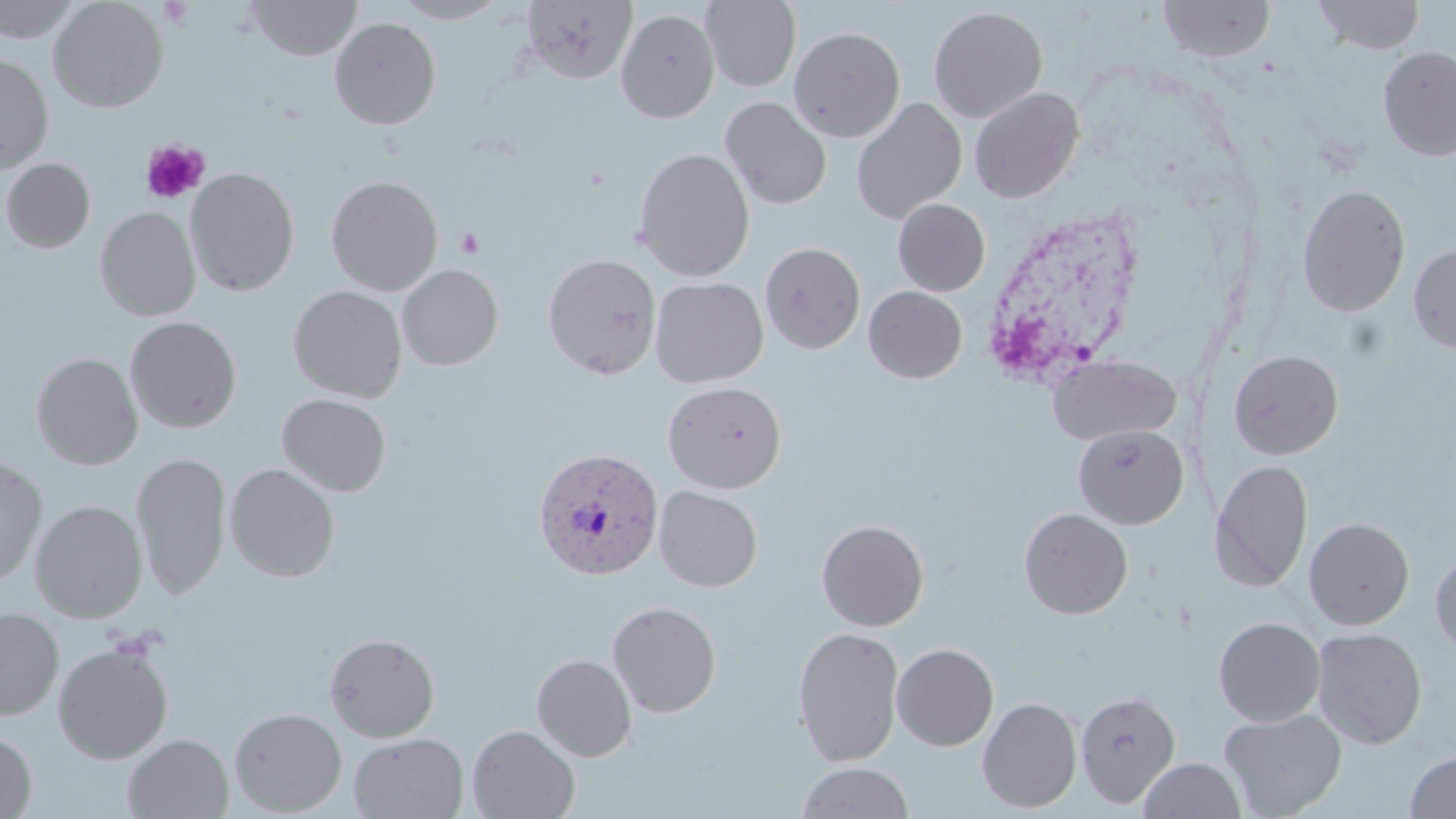
Summary:
  - Coordinate format: approximate bounding boxes as (x1,y1)-(x2,y2) corner pairs in pixels
  - Uninfected red blood cell locations: (48,0)-(168,113), (247,0)-(361,60), (392,0)-(507,23), (520,0)-(637,84), (701,0)-(800,91), (1159,0)-(1274,61), (1314,0)-(1424,54), (0,1)-(81,44), (929,6)-(1048,123), (616,9)-(719,123), (330,17)-(440,129), (789,26)-(904,142), (1378,46)-(1456,160), (0,55)-(54,173), (968,87)-(1085,203), (721,97)-(832,209), (850,98)-(967,225), (633,148)-(755,282), (0,158)-(95,252), (185,167)-(299,296), (326,175)-(443,296), (1297,184)-(1410,316), (893,199)-(990,296), (95,206)-(200,321), (760,243)-(865,354), (1408,244)-(1456,353), (543,254)-(662,379), (397,264)-(503,370), (649,277)-(768,388), (288,285)-(407,403), (864,286)-(966,383), (125,316)-(241,433), (1228,350)-(1343,459), (31,352)-(143,470), (1047,354)-(1181,445), (662,381)-(786,493), (277,394)-(391,497), (1073,424)-(1189,529), (131,452)-(231,599), (0,455)-(47,590), (1209,459)-(1313,592), (225,463)-(340,582), (654,485)-(762,591), (30,500)-(147,623), (1019,508)-(1133,619), (1304,517)-(1414,629), (816,520)-(928,631), (1430,552)-(1456,655), (608,601)-(721,717), (0,608)-(64,720), (1214,617)-(1325,726), (792,627)-(904,766), (1311,627)-(1427,749), (324,632)-(439,742), (53,641)-(173,764), (891,643)-(998,750), (531,653)-(637,761), (1075,689)-(1181,808), (977,696)-(1082,813), (229,708)-(347,816), (1218,708)-(1347,819), (467,725)-(579,819), (0,731)-(37,818), (348,732)-(468,818), (123,733)-(234,818), (1404,750)-(1456,818), (1139,758)-(1243,818), (798,762)-(914,819)
  - Platelet locations: (141,141)-(210,204), (456,228)-(484,257)
  - Plasmodium vivax-infected red blood cell locations: (531,447)-(663,581)
  - Slide-level diagnosis: Plasmodium vivax
  - Image size: 1456×819 pixels
  - Magnification: 1000x
  - Stain: May-Grünwald-Giemsa
  - Field of view: one of a larger specimen
  - Modality: optical microscopy
  - Preparation: thin blood film